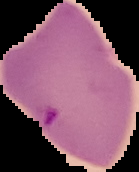

Summary:
  - Image type: cell region segmented out of the field of view; surrounding area masked to black
  - Preparation: thin blood smear
  - Image size: 139×172 pixels
  - Malaria status: parasitized